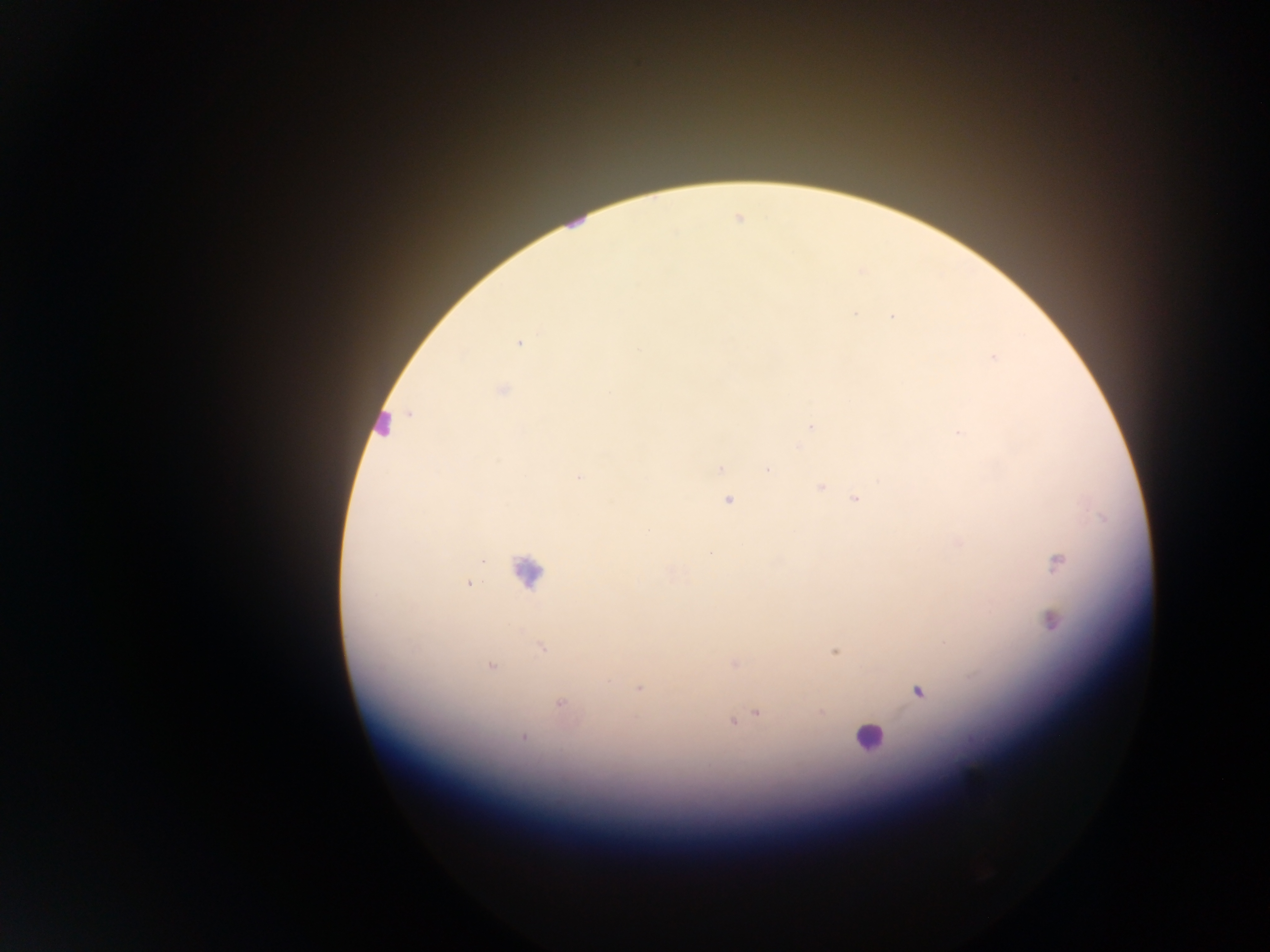

Approximate centers as x y in pixels.
Summary:
  - Malaria parasite locations: 855 315; 892 316; 518 344; 994 358; 503 390; 812 427; 961 433; 721 468; 768 469; 579 477; 820 487; 856 500; 728 501; 1057 563; 469 584; 1053 621; 542 647; 835 651; 734 663; 491 667; 610 681; 638 688; 918 690; 560 703; 821 713; 757 714; 732 722; 523 736
  - Leukocyte locations: 383 425; 527 571; 868 736
  - Field of view: single
  - Capture: mobile-phone photograph through a microscope
  - Preparation: thick blood film
  - Image size: 1270×952 pixels
  - Country: Ghana